State which cell type is depicted.
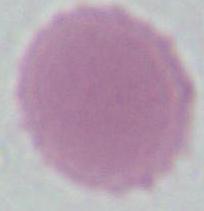
An erythrocyte.

{
  "magnification": "1000x",
  "modality": "photomicrograph"
}